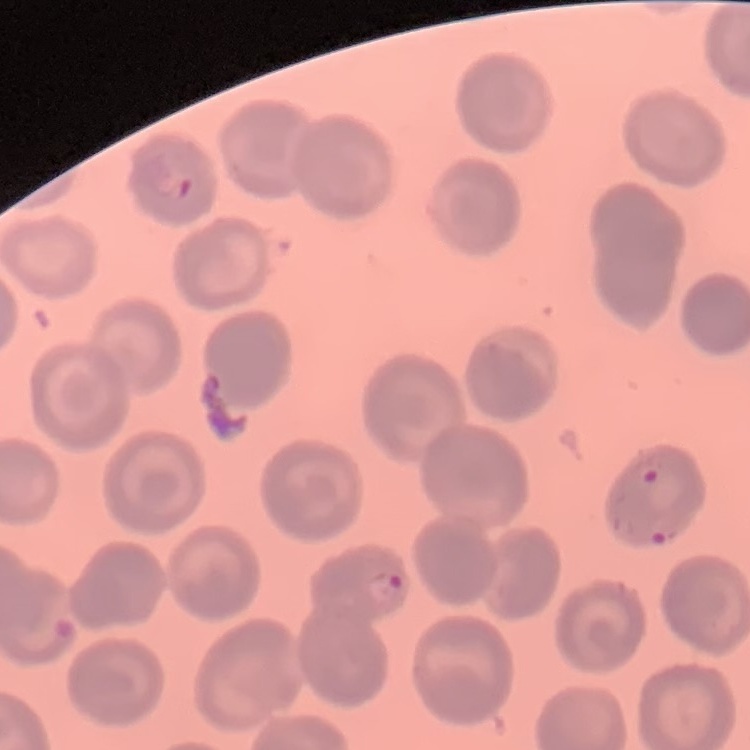

Summary:
  - Erythrocyte morphology: no rouleaux formation
  - Image type: square crop of a larger photomicrograph
  - Preparation: thin blood film
  - Stain: Field's or Giemsa